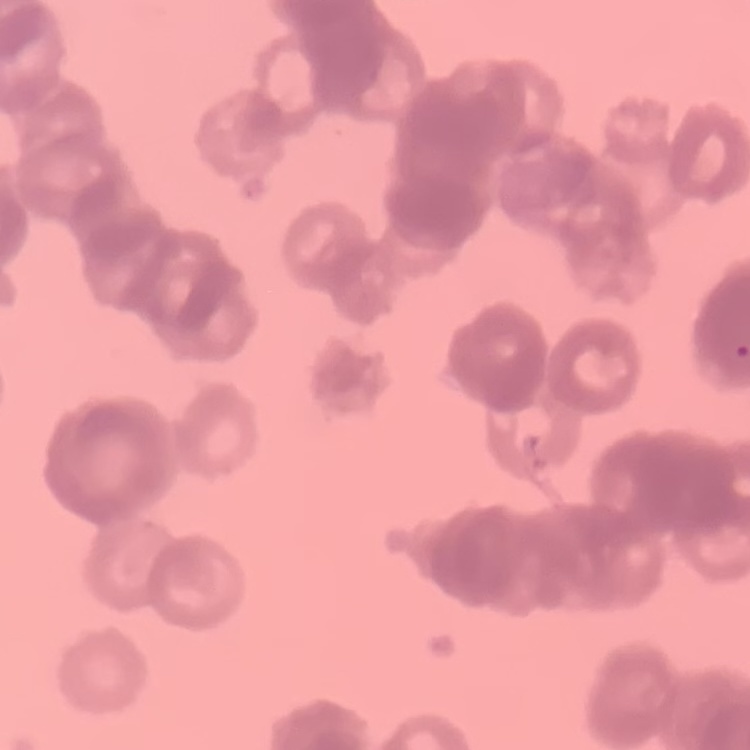
The erythrocytes exhibit rouleaux formation. Square crop of a larger photomicrograph. Field's or Giemsa stain. Thin blood smear.